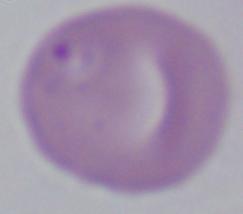

{
  "modality": "photomicrograph",
  "magnification": "1000x",
  "identification": "Babesia"
}